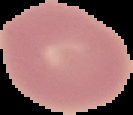
Summary:
  - Preparation: thin blood film
  - Image type: segmented cell region with the area outside set to black
  - Result: negative for malaria parasites
  - Image size: 133×115 pixels